Assess this cell for malaria.
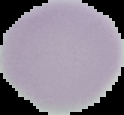
It is uninfected.

Summary:
  - Preparation: thin blood smear
  - Image type: segmented cell region on a black background
  - Image size: 124×115 pixels